Describe the morphology of the red blood cells.
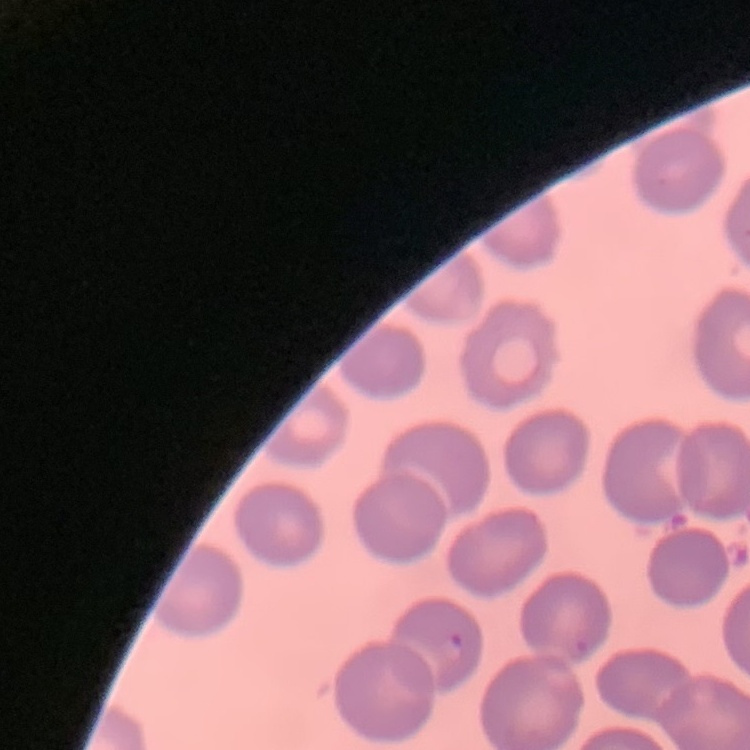
No rouleaux formation.

image_type: one tile cut from a larger photomicrograph
stain: Field's or Giemsa
preparation: thin peripheral smear